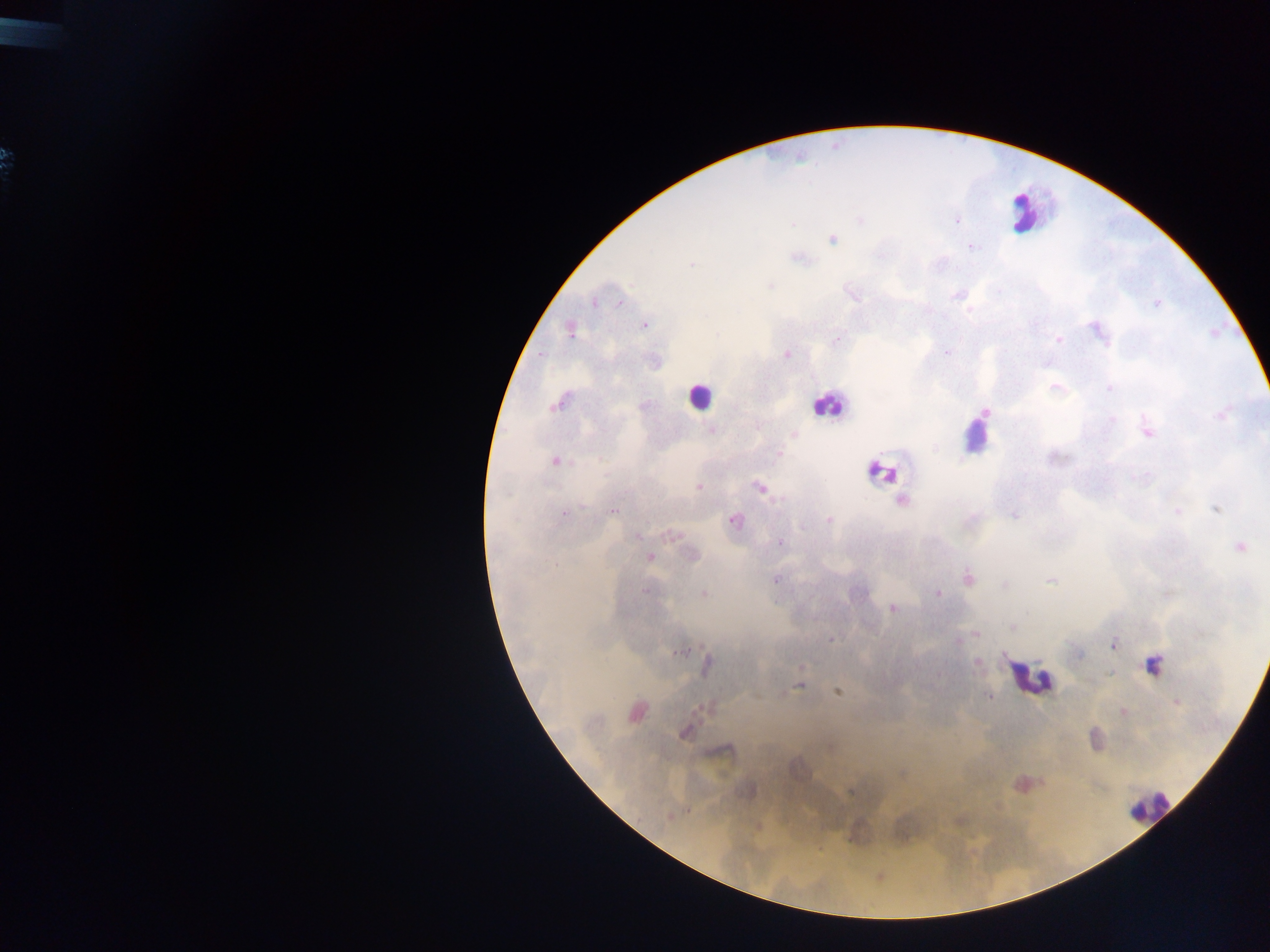 Approximate centers as (x, y) in pixels. Plasmodium parasite locations: (861, 220), (957, 221), (792, 224), (832, 239), (971, 247), (799, 258), (691, 264), (770, 286), (852, 294), (957, 296), (594, 303), (1157, 303), (620, 304), (969, 310), (644, 325), (1097, 330), (570, 331), (836, 340), (1058, 340), (947, 351), (787, 354), (540, 356), (1055, 387), (1109, 388), (557, 404), (985, 411), (1221, 415), (1112, 419), (712, 430), (1147, 431), (794, 435), (778, 453), (556, 461), (1137, 477), (699, 487), (759, 488), (901, 500), (582, 505), (1216, 508), (613, 511), (1177, 512), (565, 513), (1014, 514), (829, 520), (735, 521), (669, 535), (636, 536), (780, 543), (1241, 547), (692, 554), (650, 557), (968, 577), (776, 579), (1050, 581), (1005, 585), (645, 591), (703, 593), (938, 594), (892, 608), (1011, 627), (976, 633), (965, 638), (832, 639), (958, 641), (1114, 644), (680, 652), (1079, 654), (978, 662), (707, 665), (1153, 665), (800, 685), (837, 692), (989, 697), (1176, 702), (704, 707), (636, 711), (1123, 712), (684, 732), (725, 750), (901, 775), (851, 792), (686, 811), (668, 816). Leukocyte locations: (1022, 213), (699, 396), (828, 405), (976, 440), (882, 475), (1030, 677), (1149, 806). Single field of view. Collected in Ghana. Thick blood film. Mobile-phone photograph taken through the microscope. Image is 1270×952 pixels.